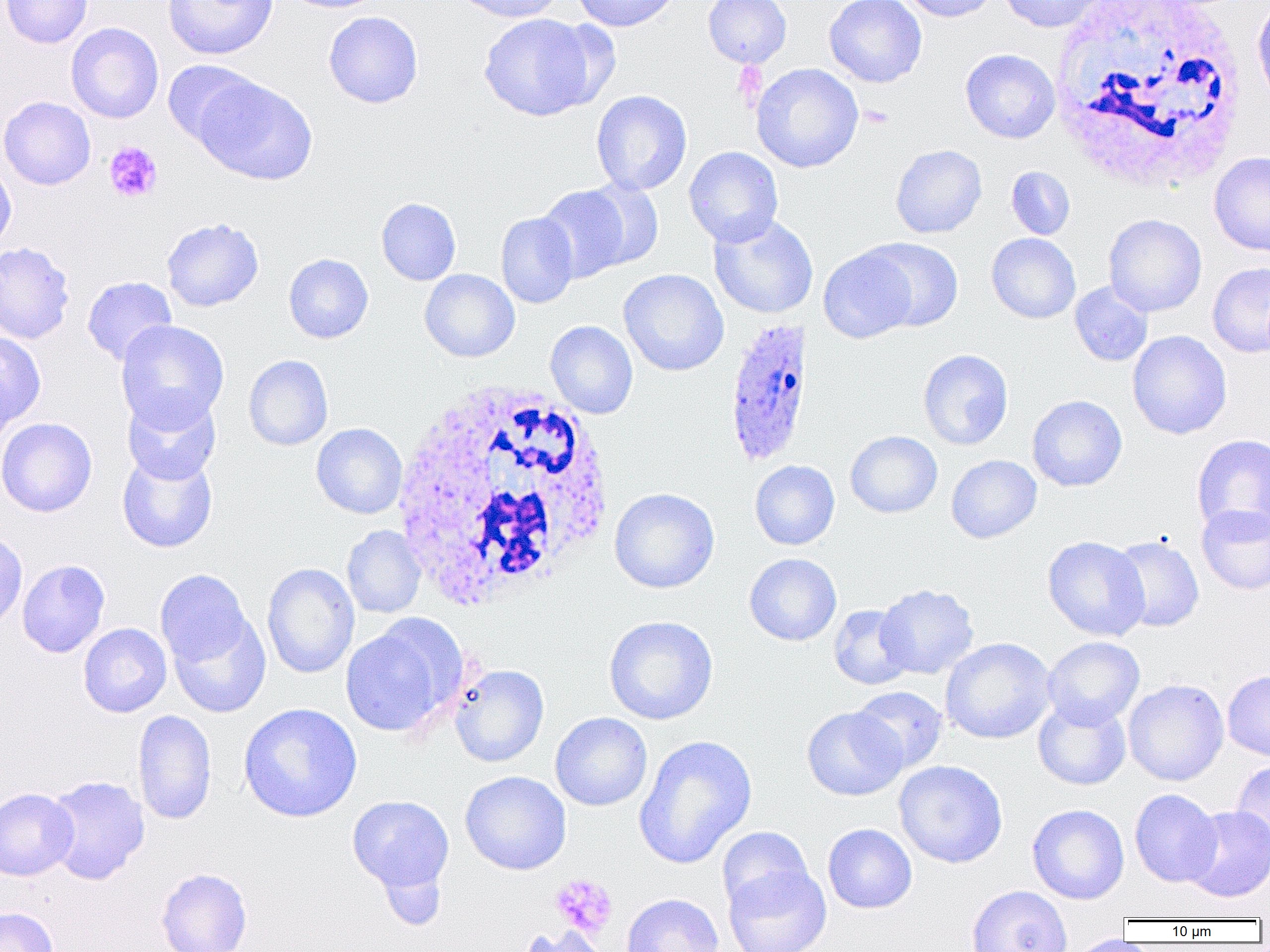
Approximate bounding boxes as [x1, y1, x2, y2] in pixels. White blood cell locations: [1048, 0, 1249, 192], [390, 380, 616, 610]. Plasmodium ovale-infected red blood cell locations: [723, 317, 816, 467]. Platelet locations (subset): [860, 105, 893, 128], [104, 141, 163, 203], [550, 874, 617, 937]. Uninfected red blood cell locations (subset): [1, 0, 93, 48], [163, 0, 277, 59], [280, 0, 390, 13], [452, 0, 566, 23], [572, 0, 680, 31], [703, 0, 791, 67], [824, 0, 927, 88], [895, 0, 1000, 22], [998, 0, 1108, 33], [1251, 2, 1270, 110], [323, 11, 424, 109], [479, 13, 597, 121], [66, 22, 164, 123], [960, 49, 1061, 143], [162, 60, 260, 149], [751, 63, 863, 173], [196, 76, 317, 185], [591, 90, 692, 195], [890, 144, 987, 238], [684, 146, 783, 247], [1209, 151, 1270, 257], [0, 158, 17, 253], [1006, 166, 1075, 240], [582, 179, 664, 270], [536, 185, 633, 283], [376, 197, 461, 285], [495, 212, 579, 308], [708, 213, 818, 320], [1104, 214, 1207, 316], [161, 216, 264, 312], [986, 233, 1080, 324], [862, 238, 963, 332], [0, 241, 76, 345], [818, 245, 919, 343], [283, 253, 373, 343], [1207, 262, 1270, 357], [618, 268, 729, 376], [419, 269, 520, 362], [81, 276, 177, 366], [1069, 281, 1153, 366], [115, 320, 229, 431], [545, 320, 638, 419], [1127, 330, 1232, 439], [0, 331, 46, 431], [918, 349, 1013, 450], [243, 354, 333, 451], [122, 391, 222, 485], [1027, 395, 1127, 491], [0, 416, 97, 517], [311, 423, 407, 519], [845, 430, 943, 518], [1191, 434, 1270, 537], [117, 451, 218, 553], [946, 455, 1042, 543], [750, 460, 840, 550], [609, 487, 720, 593], [1197, 505, 1270, 595], [342, 525, 426, 618], [0, 528, 28, 632], [1042, 535, 1150, 641], [1109, 535, 1205, 633], [744, 553, 842, 646], [17, 559, 110, 658], [262, 562, 359, 679], [155, 569, 253, 667], [876, 584, 978, 679], [828, 604, 915, 690], [166, 609, 271, 718], [604, 615, 718, 725], [340, 619, 461, 737], [78, 623, 172, 718], [1042, 636, 1145, 728], [940, 637, 1056, 744], [449, 664, 550, 767], [1222, 670, 1270, 760], [1123, 679, 1229, 786], [850, 686, 948, 774], [1033, 698, 1131, 790], [238, 702, 363, 823], [802, 706, 907, 800], [133, 709, 217, 825], [550, 712, 652, 811], [633, 735, 757, 869], [894, 760, 1008, 868], [1230, 760, 1270, 856], [460, 771, 571, 875], [44, 775, 150, 885], [0, 788, 79, 880], [1129, 788, 1222, 887], [347, 795, 454, 893], [1027, 803, 1129, 904], [1182, 805, 1270, 902], [823, 823, 917, 913], [717, 827, 813, 914], [377, 862, 448, 930], [723, 863, 831, 952], [156, 868, 252, 952], [550, 872, 618, 941], [966, 884, 1072, 952], [621, 893, 723, 952], [0, 906, 58, 952], [516, 925, 609, 952], [1067, 934, 1138, 952]. Slide-level diagnosis: Plasmodium ovale. Single field of view. Image is 1270×952 pixels. Captured at 1000x magnification. Thin blood smear. Light microscopy.